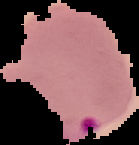

preparation = thin blood film
image size = 139×145 pixels
malaria status = parasitized
image type = cell region segmented out of the field of view; surrounding area masked to black